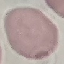
Summary:
  - Result: no malaria parasites seen
  - Capture: smartphone through the microscope eyepiece
  - Image type: automatically extracted cell patch, resized to 64 × 64 pixels
  - Preparation: thin blood film
  - Stain: Giemsa